Report the malaria status of this cell.
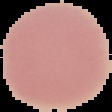
It is uninfected.

{
  "image_size": "112×112 pixels",
  "preparation": "thin blood film",
  "image_type": "segmented cell region with the area outside set to black"
}